State the preparation type.
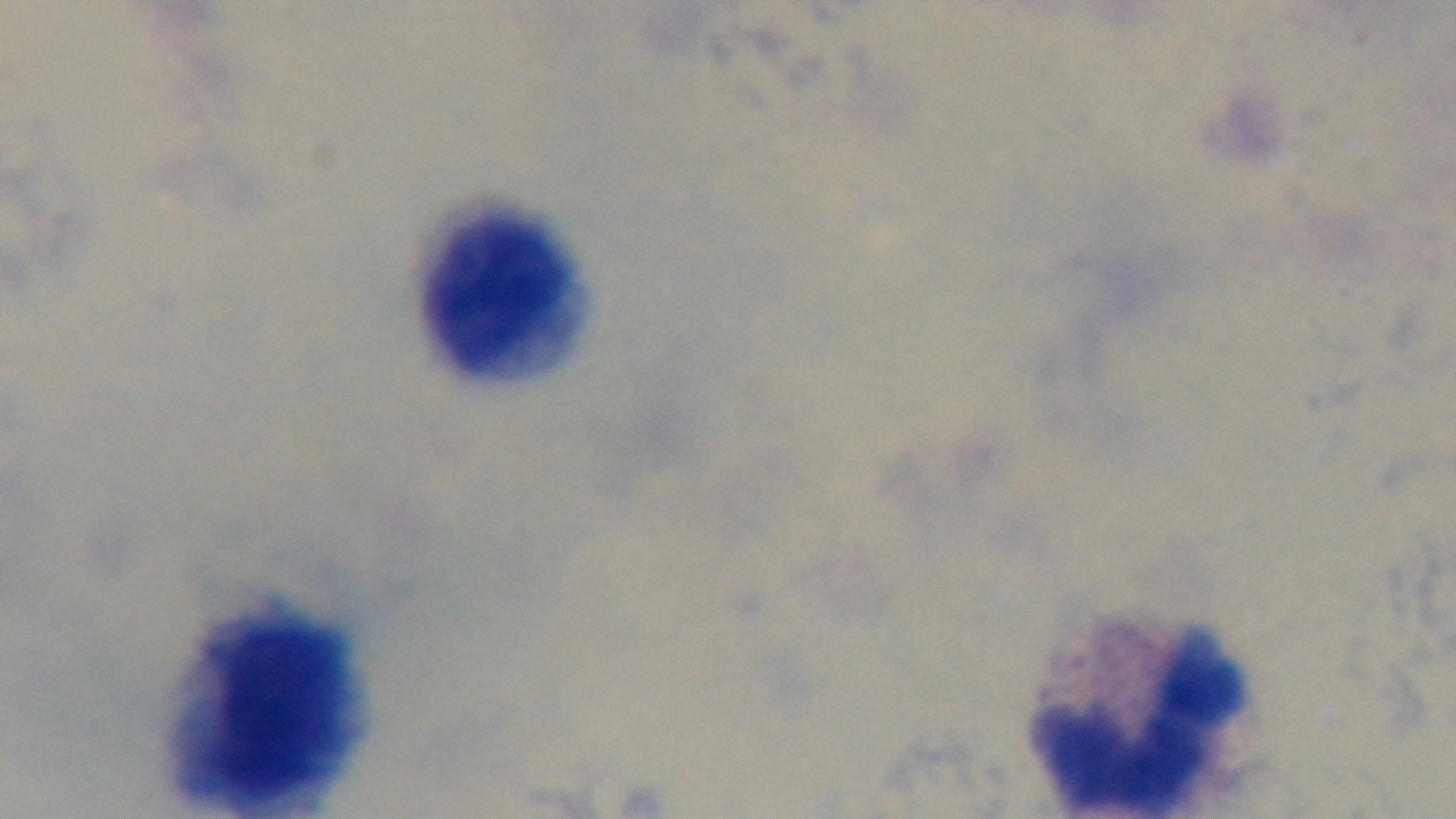
A thick smear.

capture = mounted 4K digital camera
objective = 100x oil immersion
modality = light microscopy
stain = Giemsa
malaria status = negative
field of view = one from the slide